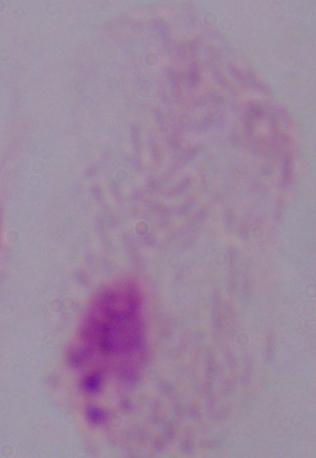 Captured at 1000x magnification. Micrograph. A trichomonad is seen.